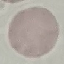
malaria_status: uninfected
preparation: thin blood film
image_type: automatically extracted cell patch, resized to 64 × 64 pixels
capture: smartphone camera at the microscope eyepiece
stain: Giemsa